State which parasite is depicted.
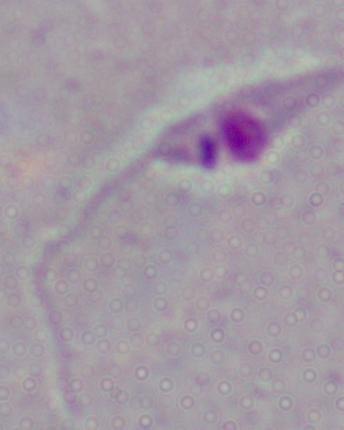
Leishmania.

Photomicrograph. 1000x magnification.